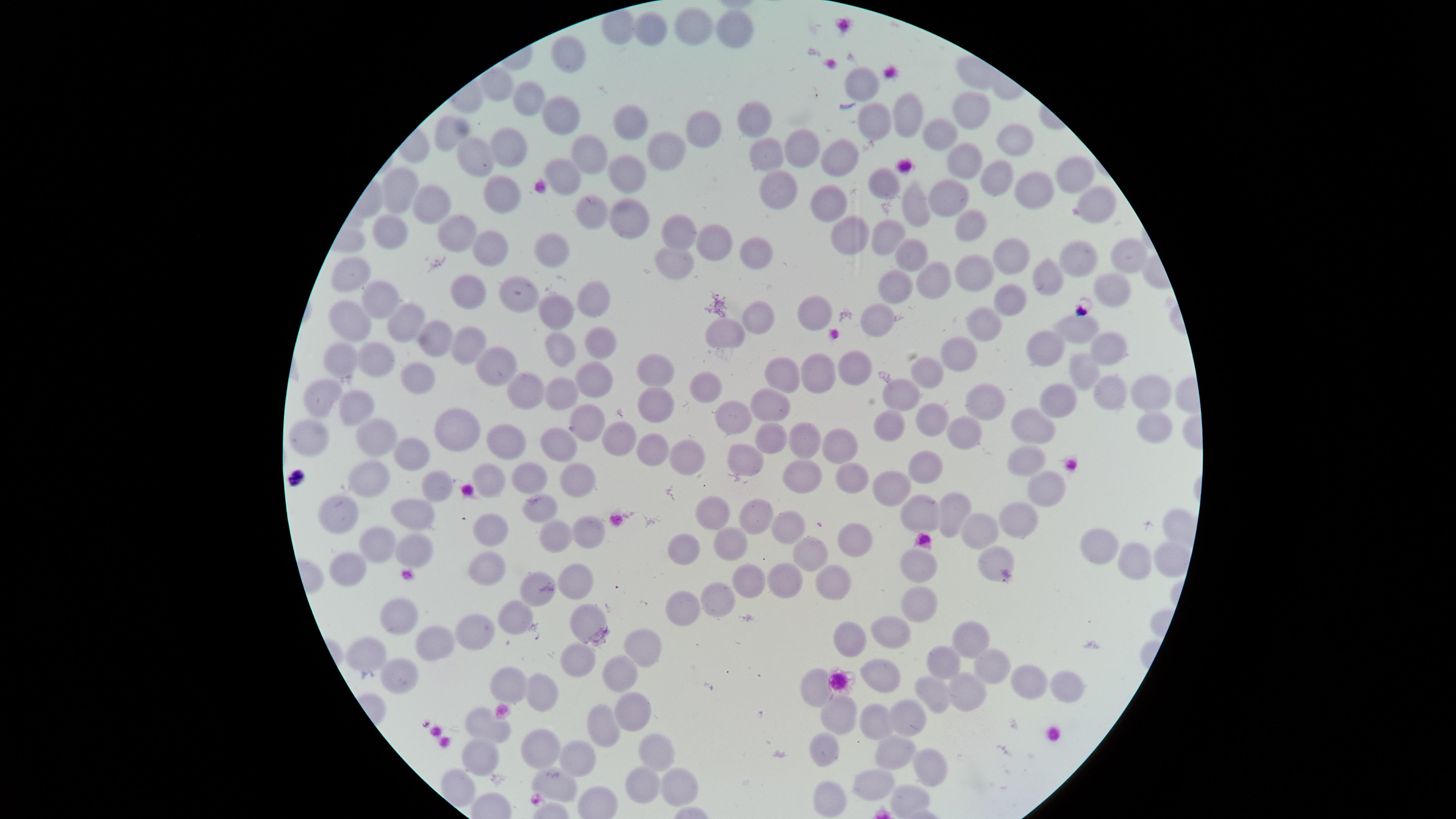 Approximate marker points as [x, y] in pixels. Uninfected red blood cells: [692, 25], [648, 27], [735, 32], [569, 56], [859, 80], [527, 98], [974, 107], [561, 113], [759, 117], [900, 119], [625, 127], [699, 129], [868, 129], [447, 132], [1011, 135], [940, 137], [501, 142], [800, 144], [668, 150], [588, 152], [760, 153], [834, 158], [472, 159], [963, 161], [558, 170], [991, 178], [1068, 180], [625, 184], [882, 184], [392, 186], [1035, 186], [774, 190], [497, 194], [1086, 200], [828, 201], [949, 203], [430, 205], [909, 205], [588, 207], [624, 216], [678, 227], [967, 227], [452, 228], [848, 234], [887, 234], [387, 235], [713, 243], [552, 249], [487, 250], [751, 252], [1010, 253], [909, 255], [1121, 255], [1075, 258], [675, 259], [976, 271], [349, 276], [1046, 277], [922, 279], [519, 283], [465, 285], [1103, 286], [885, 289], [591, 294], [1014, 297], [372, 301], [556, 311], [821, 312], [983, 318], [410, 319], [758, 319], [350, 323], [879, 325], [1083, 327], [728, 333], [436, 341], [596, 343], [463, 345], [1105, 345], [563, 349], [1057, 351], [958, 352], [369, 357], [339, 364], [493, 366], [419, 367], [1081, 367], [850, 369], [778, 373], [930, 375], [654, 376], [595, 377], [813, 379], [704, 382], [517, 386], [1145, 388], [561, 389], [903, 392], [1111, 392], [1054, 393], [319, 396], [984, 398], [357, 402], [770, 404], [655, 411], [741, 411], [928, 414], [581, 419], [1153, 421], [887, 424], [964, 429], [1030, 429], [310, 430], [452, 432], [619, 432], [773, 433], [506, 435], [373, 437], [558, 441], [803, 441], [839, 441], [649, 446], [745, 450], [407, 451], [1032, 452], [675, 453], [929, 465], [369, 472], [846, 472], [531, 473], [492, 476], [800, 478], [898, 478], [575, 483], [1048, 484], [431, 485], [717, 502], [953, 504], [544, 506], [753, 509], [341, 511], [414, 511], [921, 512], [1009, 517], [785, 519], [587, 526], [487, 527], [981, 530], [549, 535], [845, 536], [366, 540], [413, 545], [1107, 545], [680, 547], [728, 547], [814, 548], [923, 560], [1139, 560], [1167, 561], [987, 564], [347, 565], [486, 566], [578, 578], [787, 578], [749, 579], [826, 581], [534, 586], [717, 596], [924, 600], [679, 608], [514, 613], [399, 614], [582, 620], [479, 621], [898, 624], [846, 633], [981, 639], [430, 644], [643, 645], [362, 648], [946, 658], [571, 660], [993, 663], [619, 671], [882, 675], [397, 677], [508, 679], [819, 679], [1023, 679], [1063, 684], [930, 689], [964, 690], [538, 692], [632, 702], [881, 715], [839, 716], [907, 718], [602, 725], [489, 729], [539, 738], [824, 742], [656, 749], [896, 750], [473, 753], [573, 754], [923, 765], [872, 775], [549, 777], [633, 782], [456, 783], [672, 783], [904, 793], [823, 796]. Circular visible region. Image is 1456×819 pixels. Smartphone photograph through the microscope eyepiece. One field of view of the specimen. Thin blood smear. Presence: no malaria parasites detected. Giemsa stain.